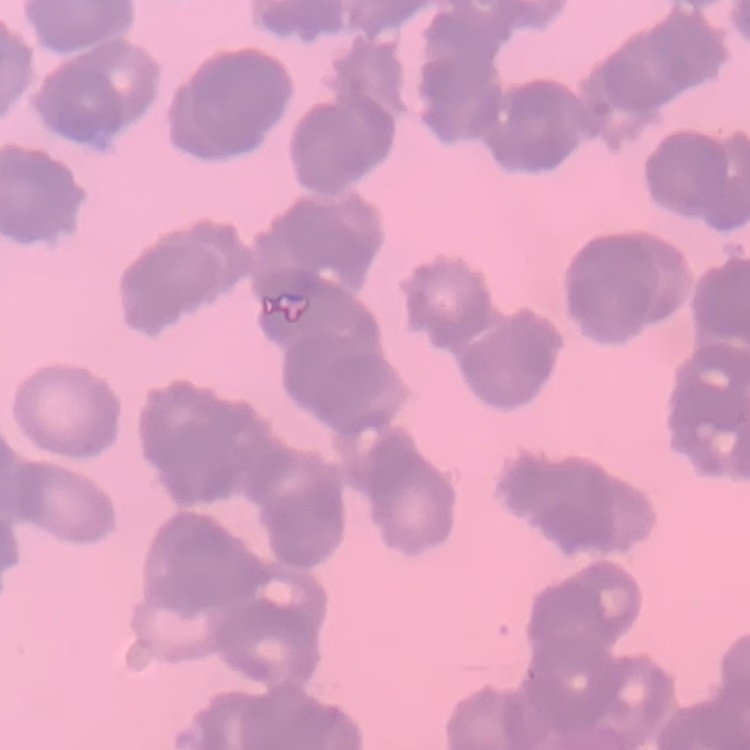

The erythrocytes exhibit rouleaux formation. Thin blood film. Stained with either Field's or Giemsa. One tile cut from a larger photomicrograph.